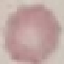

Summary:
  - Result: no malaria parasites detected
  - Image type: automatically extracted cell patch, resized to 64 × 64 pixels
  - Capture: smartphone camera at the microscope eyepiece
  - Stain: Giemsa
  - Preparation: thin smear